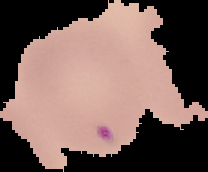

Summary:
  - Image size: 208×172 pixels
  - Preparation: thin blood film
  - Result: no Plasmodium parasites detected
  - Image type: segmented cell region with the area outside set to black